Locate every blood parasite and identify its species.
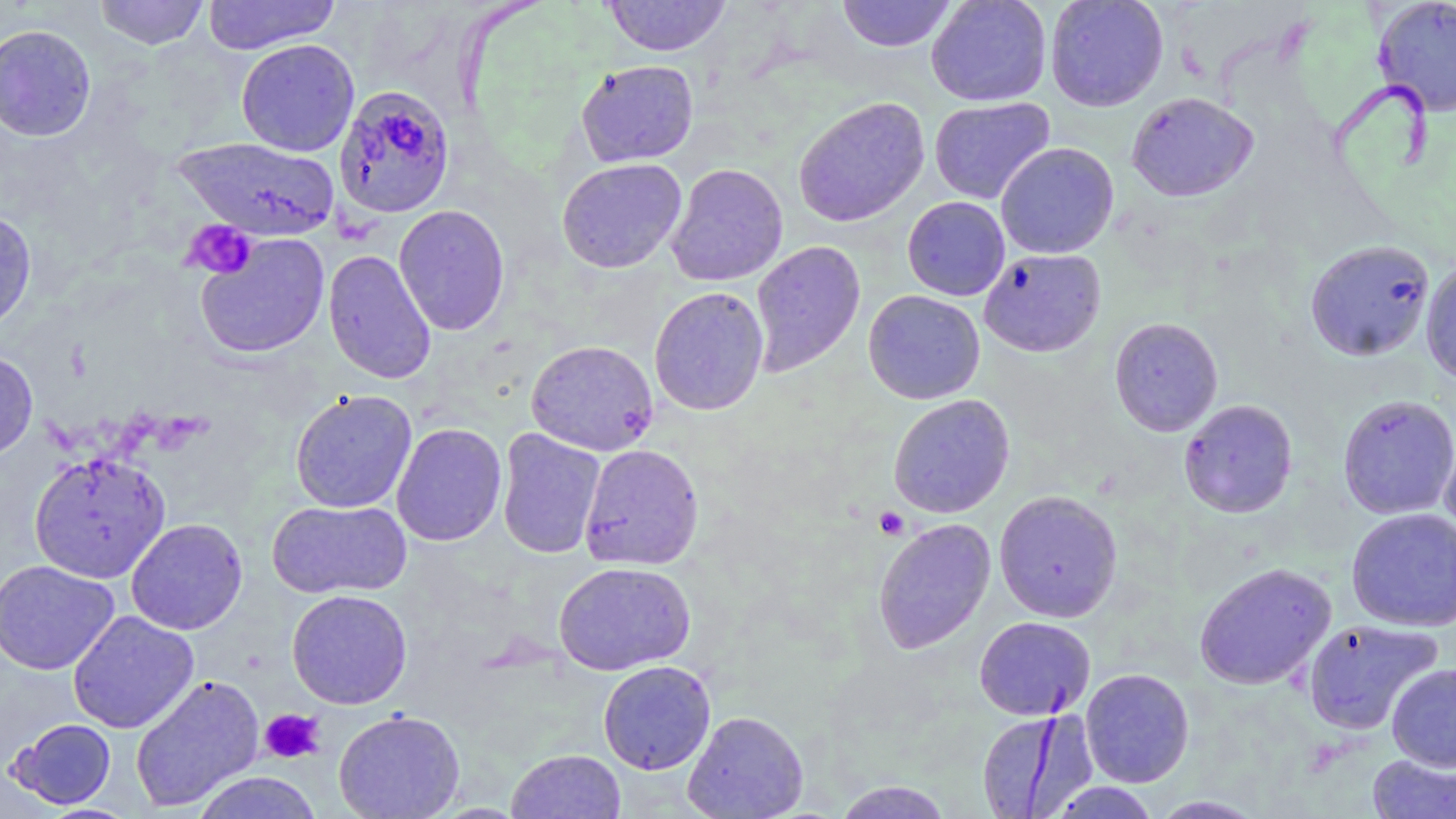

Approximate bounding boxes as [x1, y1, x2, y2] in pixels.
Plasmodium falciparum-infected red blood cells: [333, 84, 456, 218].
No Plasmodium ovale, Plasmodium malariae, Plasmodium vivax, Babesia divergens, or Trypanosoma brucei observed.

slide-level diagnosis = Plasmodium falciparum
preparation = thin blood smear
field of view = one of a larger specimen
modality = optical microscopy
image size = 1456×819 pixels
magnification = 1000x
platelet locations = approximate bounding boxes as [x1, y1, x2, y2] in pixels: [182, 218, 257, 279], [874, 506, 910, 540], [259, 709, 325, 764]
uninfected red blood cell locations = approximate bounding boxes as [x1, y1, x2, y2] in pixels: [94, 0, 210, 50], [203, 0, 340, 55], [602, 0, 732, 57], [836, 0, 957, 53], [926, 0, 1052, 107], [1045, 0, 1168, 112], [1373, 0, 1456, 117], [0, 24, 97, 142], [236, 38, 360, 156], [576, 60, 699, 167], [1126, 92, 1257, 202], [792, 96, 930, 228], [929, 97, 1055, 204], [175, 136, 341, 241], [995, 142, 1119, 259], [557, 157, 687, 273], [666, 163, 788, 286], [902, 196, 1010, 300], [393, 204, 510, 335], [0, 209, 37, 334], [194, 233, 330, 359], [1305, 239, 1435, 361], [750, 240, 866, 376], [979, 248, 1106, 358], [323, 249, 437, 384], [1421, 259, 1456, 386], [648, 286, 769, 416], [862, 290, 985, 405], [1109, 316, 1223, 437], [526, 339, 658, 456], [0, 349, 38, 461], [289, 389, 418, 513], [1337, 393, 1456, 520], [888, 394, 1015, 518], [1179, 398, 1297, 518], [391, 423, 507, 546], [496, 428, 606, 560], [1439, 432, 1456, 547], [579, 443, 704, 570], [28, 451, 170, 584], [994, 490, 1123, 622], [267, 499, 412, 598], [1346, 507, 1456, 631], [126, 518, 247, 635], [872, 518, 996, 654], [0, 559, 120, 675], [553, 561, 695, 676], [1194, 561, 1335, 690], [286, 589, 413, 709], [67, 610, 199, 734], [974, 616, 1095, 721], [1302, 618, 1443, 735], [598, 660, 715, 774], [1387, 663, 1456, 772], [1080, 668, 1194, 788], [130, 674, 265, 811], [333, 709, 466, 819], [682, 710, 809, 819], [976, 710, 1086, 818], [8, 718, 116, 809], [506, 749, 627, 819], [1368, 753, 1455, 819], [191, 771, 324, 819], [833, 780, 953, 818], [1047, 781, 1162, 819], [1149, 795, 1266, 818]
stain = May-Grünwald-Giemsa